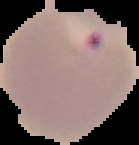

Summary:
  - Malaria status: parasitized
  - Preparation: thin blood film
  - Image type: segmented cell region on a black background
  - Image size: 139×145 pixels